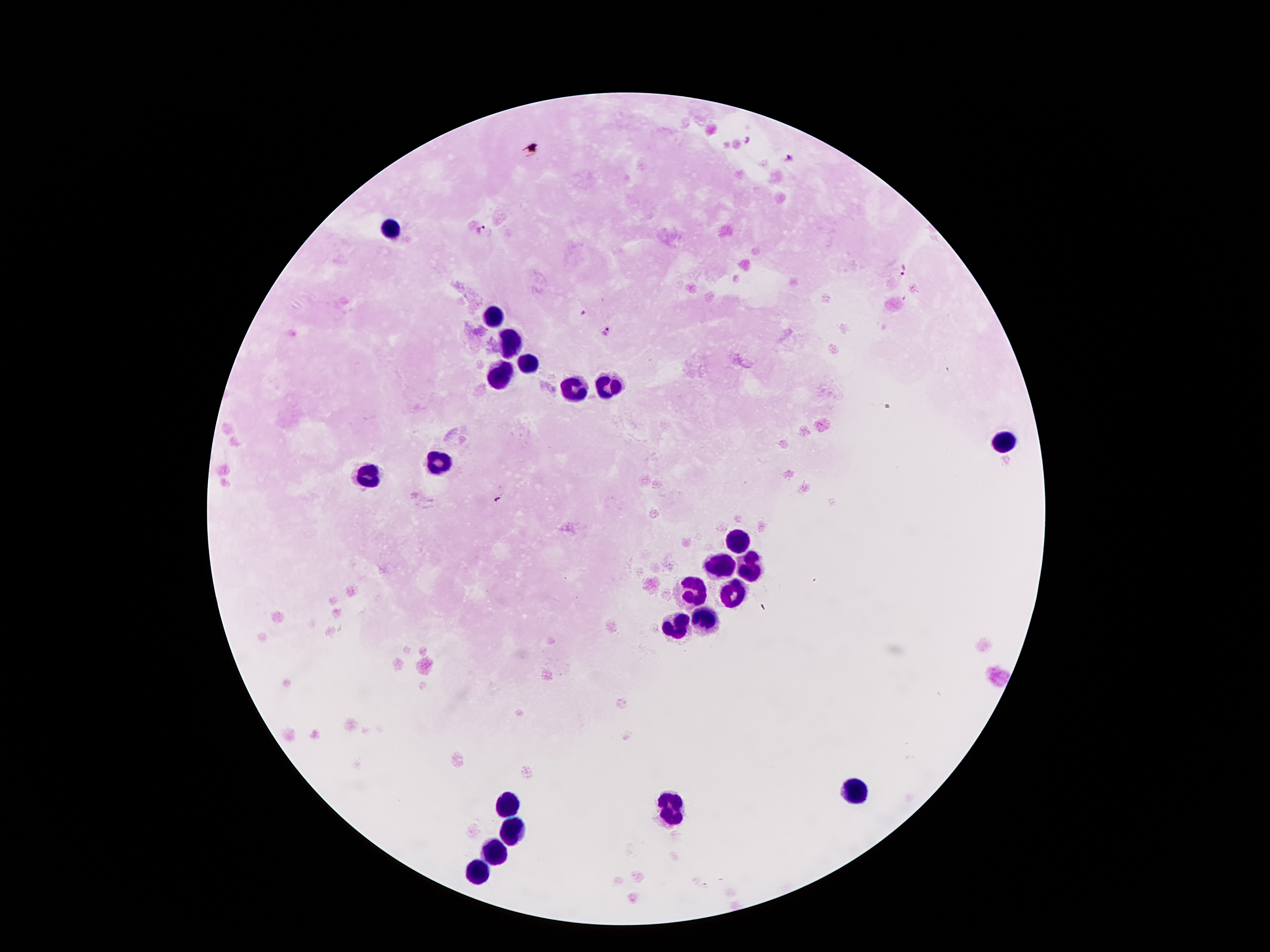
Approximate centers as {x, y} in pixels. Malaria parasite locations: {482, 229}, {903, 269}, {584, 312}, {607, 331}, {497, 499}. Leukocyte locations: {389, 229}, {494, 317}, {511, 341}, {529, 364}, {502, 371}, {609, 388}, {574, 392}, {1005, 441}, {443, 464}, {369, 476}, {735, 544}, {719, 567}, {749, 567}, {691, 588}, {726, 589}, {704, 618}, {677, 623}, {856, 791}, {509, 803}, {672, 812}, {508, 826}, {497, 852}, {480, 873}. Thick peripheral-blood smear. Giemsa stain. Patient malaria status: positive for Plasmodium falciparum. 100x magnification. One field from this slide. Image is 1270×952 pixels. Photographed through the microscope eyepiece with a smartphone camera.